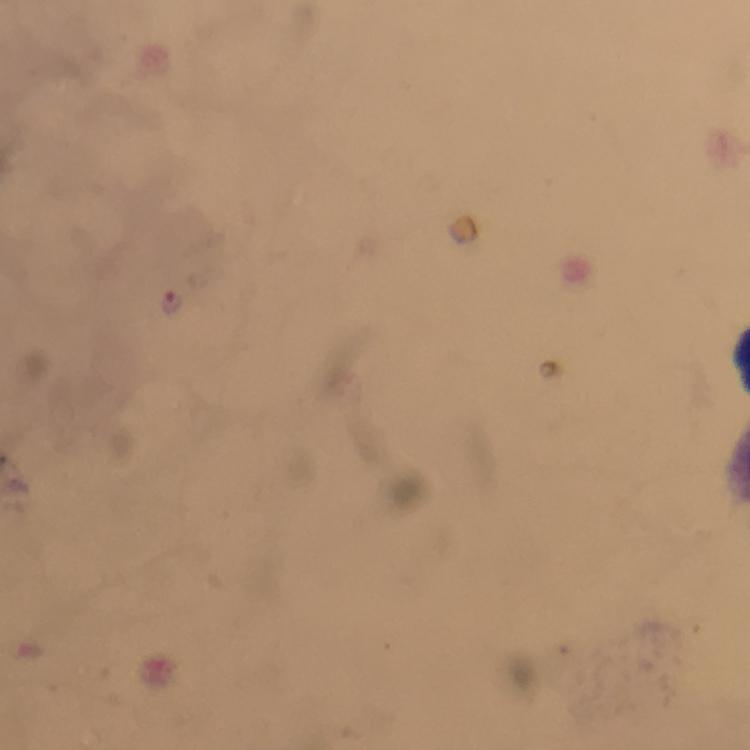

Approximate centers as [x, y] in pixels.
Summary:
  - Plasmodium parasite locations: [172, 301]
  - Stain: Giemsa
  - Context: from a diagnostic examination for malaria
  - Image size: 750×750 pixels
  - Cropped from: one field of view
  - Capture: smartphone camera through the microscope
  - Preparation: thick blood film
  - Immersion oil: applied
  - Magnification: 100x